Give the extent of all Plasmodium falciparum-infected red blood cells.
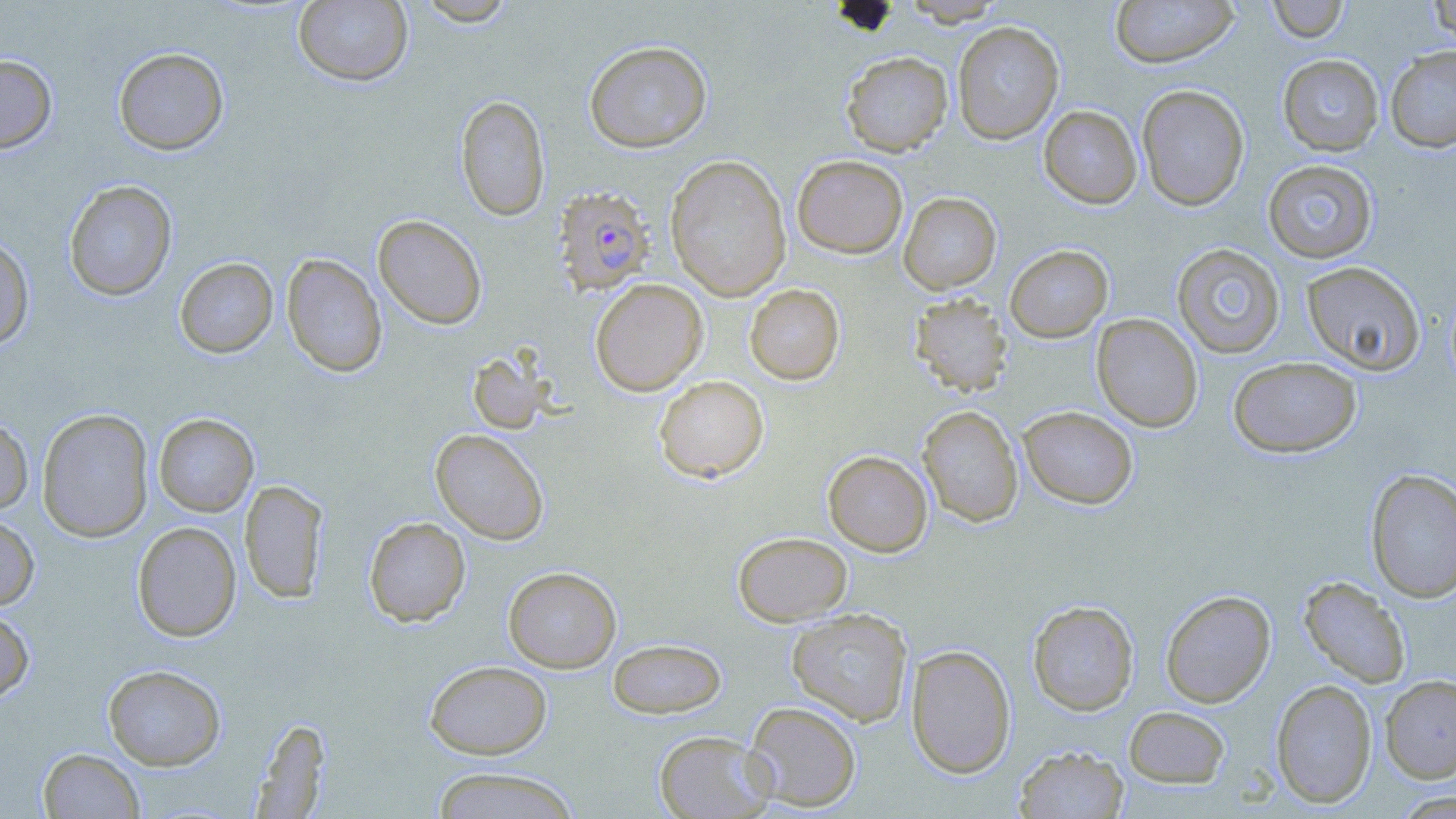

Approximate bounding boxes as named x1/y1/x2/y2 corners in pixels.
Plasmodium falciparum-infected red blood cells: (x1=551, y1=185, x2=655, y2=297).

slide-level diagnosis = Plasmodium falciparum
preparation = thin blood film
uninfected red blood cell locations = approximate bounding boxes as named x1/y1/x2/y2 corners in pixels: (x1=415, y1=0, x2=518, y2=26), (x1=901, y1=0, x2=1008, y2=25), (x1=1110, y1=0, x2=1240, y2=69), (x1=1267, y1=0, x2=1349, y2=42), (x1=1428, y1=0, x2=1456, y2=48), (x1=293, y1=1, x2=413, y2=87), (x1=952, y1=22, x2=1064, y2=144), (x1=583, y1=40, x2=713, y2=153), (x1=1385, y1=46, x2=1456, y2=153), (x1=113, y1=47, x2=229, y2=155), (x1=841, y1=51, x2=953, y2=156), (x1=0, y1=54, x2=57, y2=153), (x1=1277, y1=54, x2=1384, y2=156), (x1=1137, y1=84, x2=1250, y2=211), (x1=455, y1=95, x2=550, y2=221), (x1=1039, y1=105, x2=1142, y2=208), (x1=792, y1=154, x2=908, y2=258), (x1=665, y1=155, x2=791, y2=301), (x1=1262, y1=160, x2=1378, y2=263), (x1=63, y1=180, x2=178, y2=301), (x1=898, y1=192, x2=1001, y2=294), (x1=373, y1=214, x2=487, y2=330), (x1=0, y1=236, x2=35, y2=351), (x1=1172, y1=243, x2=1286, y2=358), (x1=1004, y1=244, x2=1113, y2=342), (x1=281, y1=253, x2=387, y2=378), (x1=174, y1=257, x2=278, y2=358), (x1=1301, y1=261, x2=1425, y2=376), (x1=590, y1=278, x2=708, y2=396), (x1=744, y1=284, x2=845, y2=385), (x1=908, y1=293, x2=1013, y2=397), (x1=1092, y1=313, x2=1203, y2=432), (x1=467, y1=349, x2=550, y2=435), (x1=1228, y1=356, x2=1361, y2=458), (x1=653, y1=375, x2=769, y2=483), (x1=917, y1=405, x2=1023, y2=527), (x1=1019, y1=406, x2=1138, y2=509), (x1=36, y1=408, x2=154, y2=542), (x1=154, y1=413, x2=259, y2=517), (x1=0, y1=415, x2=34, y2=515), (x1=430, y1=429, x2=549, y2=544), (x1=823, y1=450, x2=932, y2=557), (x1=1365, y1=469, x2=1455, y2=604), (x1=240, y1=479, x2=327, y2=604), (x1=0, y1=515, x2=39, y2=610), (x1=363, y1=516, x2=471, y2=627), (x1=132, y1=521, x2=241, y2=641), (x1=733, y1=531, x2=852, y2=626), (x1=503, y1=566, x2=621, y2=672), (x1=1298, y1=576, x2=1411, y2=688), (x1=1160, y1=590, x2=1276, y2=707), (x1=1027, y1=600, x2=1139, y2=715), (x1=0, y1=608, x2=35, y2=705), (x1=786, y1=608, x2=914, y2=727), (x1=607, y1=638, x2=726, y2=719), (x1=906, y1=644, x2=1017, y2=778), (x1=425, y1=660, x2=552, y2=759), (x1=103, y1=664, x2=226, y2=770), (x1=1380, y1=674, x2=1456, y2=783), (x1=1270, y1=678, x2=1377, y2=808), (x1=743, y1=701, x2=862, y2=812), (x1=1123, y1=706, x2=1231, y2=788), (x1=249, y1=717, x2=332, y2=817), (x1=654, y1=730, x2=775, y2=818), (x1=1014, y1=745, x2=1129, y2=818), (x1=38, y1=747, x2=145, y2=819), (x1=429, y1=766, x2=581, y2=818), (x1=1391, y1=791, x2=1456, y2=818)
stain = May-Grünwald-Giemsa
field of view = single
modality = optical microscopy
magnification = 1000x
image size = 1456×819 pixels